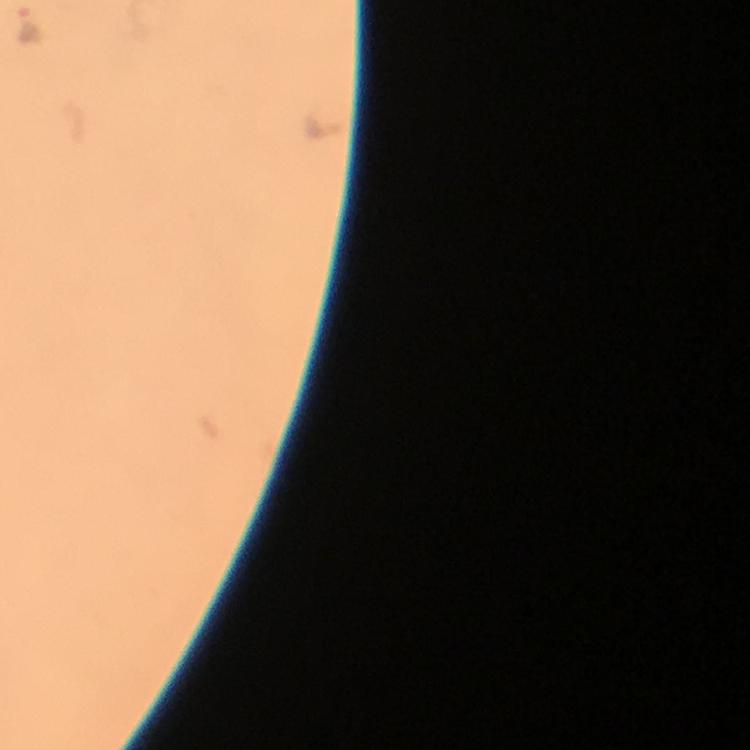
Approximate centers as (x, y) in pixels. Plasmodium parasite locations: (30, 26), (323, 124). Giemsa-stained preparation. Immersion oil applied. Smartphone photograph taken through a microscope. From a diagnostic examination for malaria. A crop from one field of view. Image is 750×750 pixels. 100x magnification. Thick blood film.